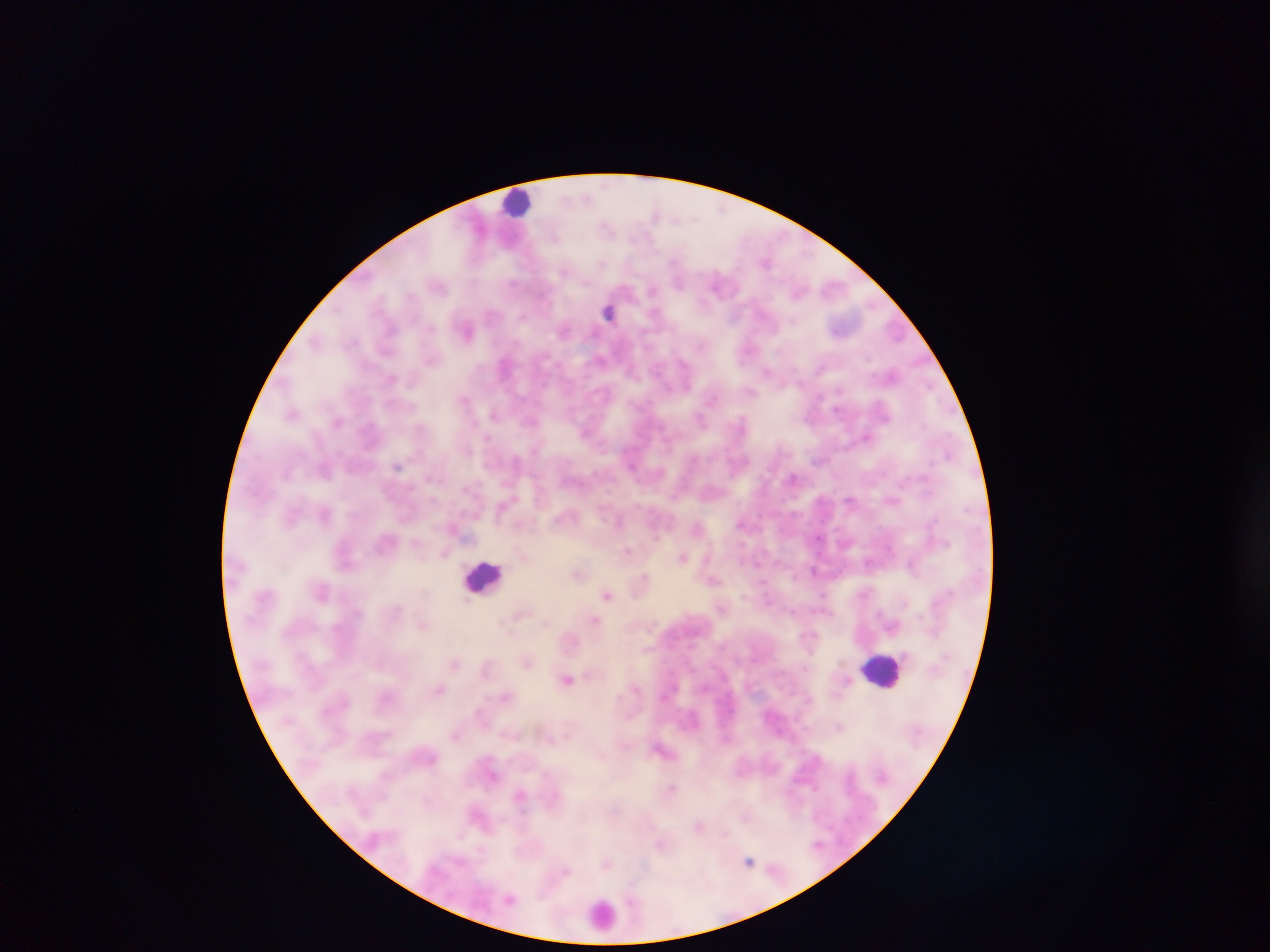

Approximate centers as [x, y] in pixels.
Summary:
  - Leukocyte locations: [519, 201], [483, 577], [882, 670], [603, 914]
  - Plasmodium parasite locations: [609, 311], [467, 328], [564, 330], [749, 347], [506, 365], [767, 371], [892, 375], [464, 398], [292, 412], [495, 414], [338, 421], [867, 436], [487, 439], [397, 465], [794, 478], [893, 500], [325, 514], [742, 523], [629, 551], [682, 556], [913, 564], [758, 565], [814, 572], [578, 573], [645, 578], [714, 580], [322, 590], [607, 594], [824, 596], [519, 614], [594, 621], [543, 623], [424, 624], [455, 662], [527, 662], [568, 679], [439, 688], [507, 695], [839, 727], [456, 734], [663, 749], [672, 789], [520, 795], [700, 827], [662, 844], [819, 845], [749, 860], [608, 863]
  - Field of view: single
  - Image size: 1270×952 pixels
  - Country: Ghana
  - Preparation: thick blood smear
  - Capture: mobile-phone photograph through a microscope